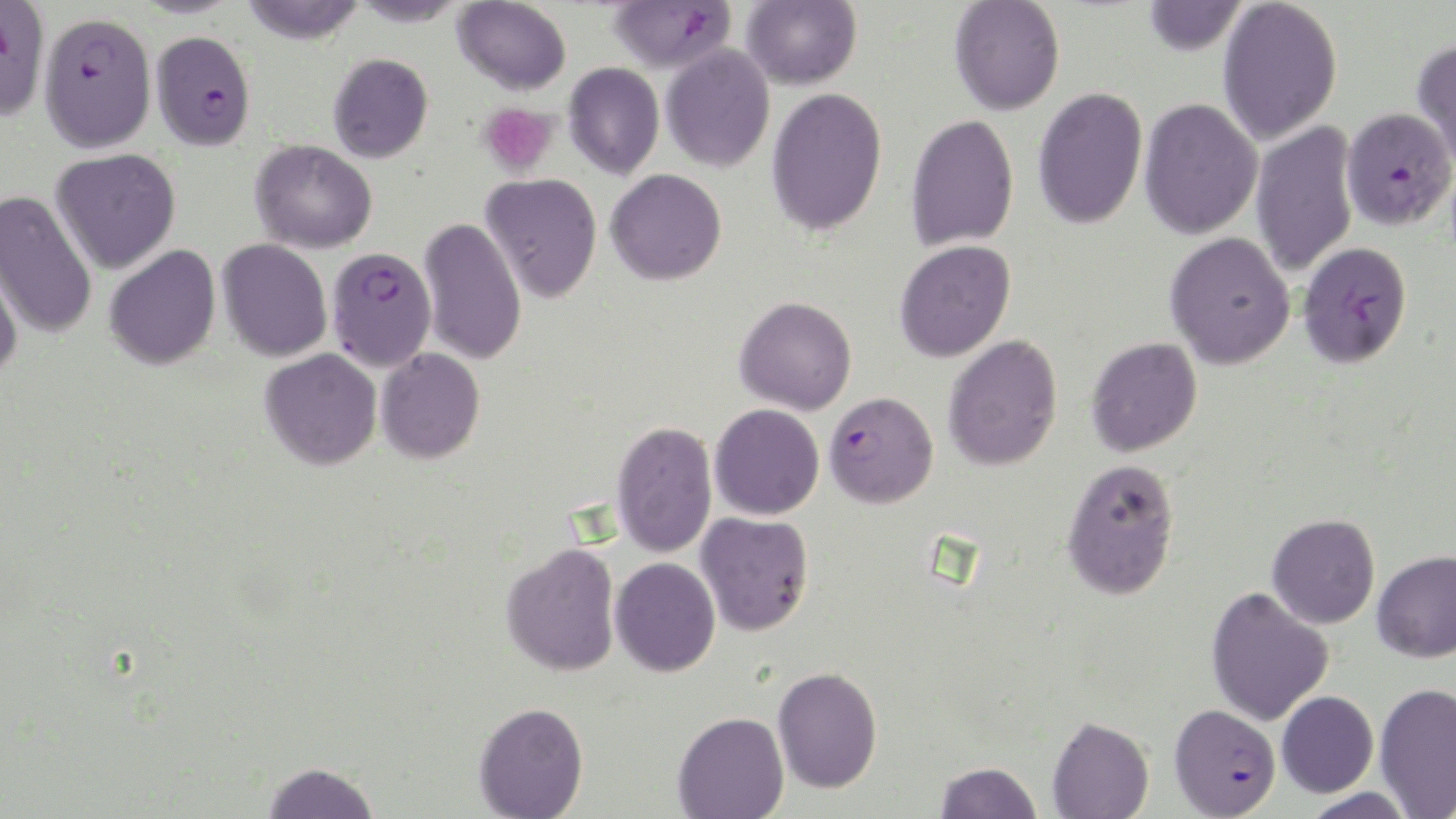
slide-level diagnosis = Plasmodium falciparum
field of view = single
image size = 1456×819 pixels
platelet locations = approximate bounding boxes as (x1,y1)-(x2,y2) corner pairs in pixels: (478,102)-(560,178)
stain = May-Grünwald-Giemsa
modality = light microscopy
uninfected red blood cell locations = approximate bounding boxes as (x1,y1)-(x2,y2) corner pairs in pixels: (239,0)-(365,43), (349,0)-(468,26), (453,0)-(571,95), (741,0)-(862,90), (949,0)-(1065,115), (1142,0)-(1247,56), (1217,0)-(1342,146), (1411,38)-(1456,170), (660,44)-(775,172), (328,53)-(433,162), (563,62)-(664,179), (766,87)-(887,236), (1032,87)-(1148,230), (1139,97)-(1263,240), (905,114)-(1019,252), (1251,120)-(1359,278), (250,140)-(378,253), (50,149)-(181,274), (606,169)-(727,285), (480,173)-(602,302), (0,190)-(98,340), (419,216)-(526,366), (1165,232)-(1295,369), (217,239)-(332,362), (894,240)-(1016,362), (104,244)-(221,370), (0,250)-(24,381), (734,296)-(857,415), (943,335)-(1063,471), (1086,337)-(1202,457), (376,348)-(485,464), (260,349)-(382,470), (709,403)-(824,520), (611,420)-(717,557), (1061,458)-(1180,600), (696,512)-(814,636), (1267,513)-(1380,629), (501,542)-(621,676), (1372,549)-(1456,663), (610,557)-(721,676), (1205,586)-(1334,727), (772,667)-(883,794), (1374,682)-(1456,816), (1276,690)-(1378,797), (473,702)-(589,819), (673,711)-(789,819), (1047,716)-(1154,819), (262,761)-(380,819), (935,761)-(1043,819), (1299,787)-(1418,819)
magnification = 1000x
Plasmodium falciparum-infected red blood cell locations = approximate bounding boxes as (x1,y1)-(x2,y2) corner pairs in pixels: (0,1)-(51,120), (606,1)-(736,73), (38,12)-(156,152), (150,31)-(256,150), (1341,107)-(1455,230), (1298,241)-(1413,368), (326,247)-(437,371), (823,391)-(938,509), (1168,704)-(1280,817)
preparation = thin blood smear